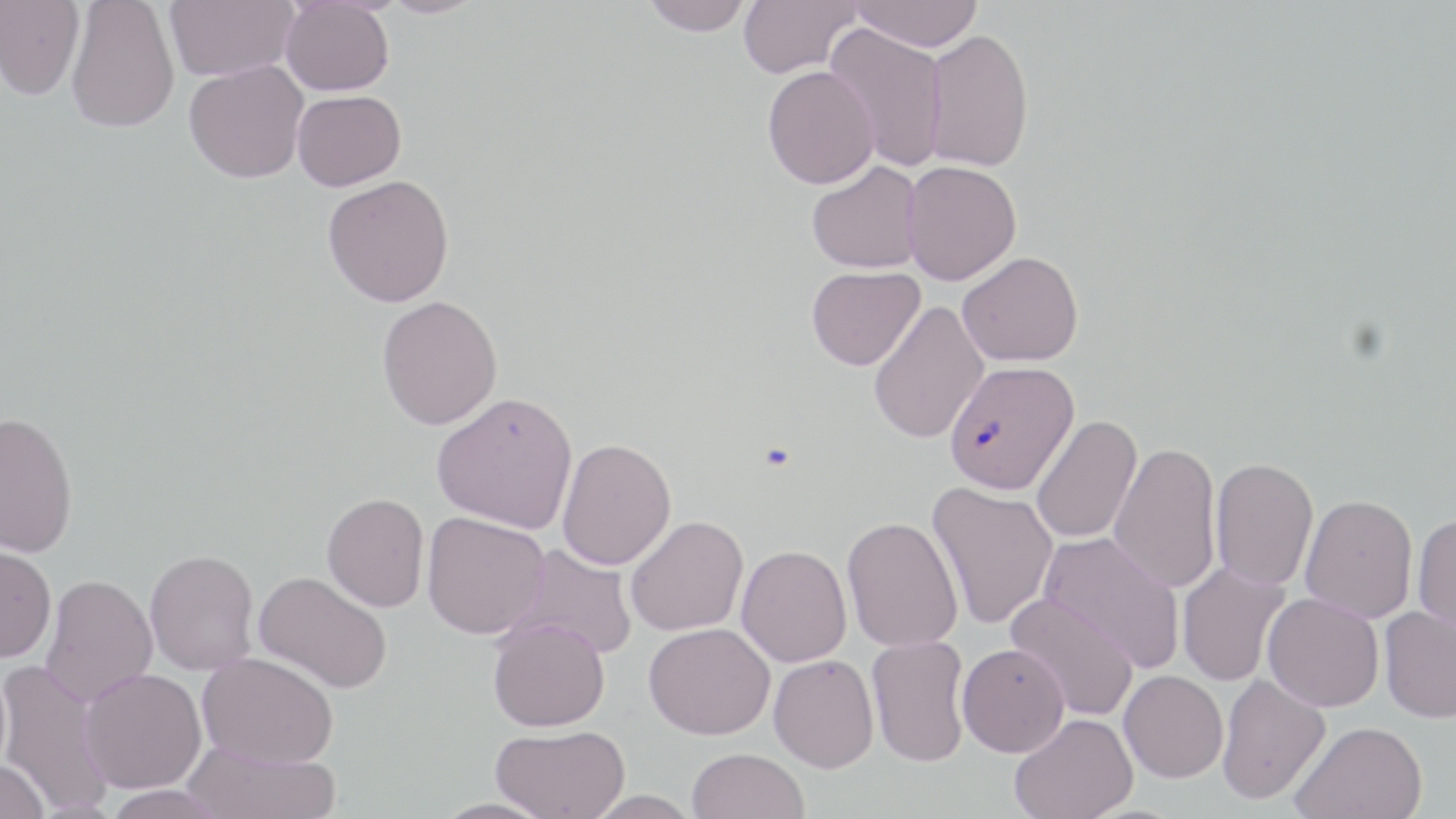

Approximate bounding boxes as named x1/y1/x2/y2 corners in pixels. Uninfected red blood cell locations: (x1=166, y1=0, x2=298, y2=81), (x1=377, y1=0, x2=486, y2=18), (x1=640, y1=0, x2=752, y2=36), (x1=738, y1=0, x2=861, y2=78), (x1=849, y1=0, x2=982, y2=52), (x1=0, y1=1, x2=85, y2=100), (x1=66, y1=1, x2=180, y2=133), (x1=281, y1=1, x2=394, y2=96), (x1=825, y1=22, x2=948, y2=173), (x1=923, y1=28, x2=1035, y2=172), (x1=184, y1=60, x2=309, y2=183), (x1=762, y1=65, x2=879, y2=189), (x1=292, y1=90, x2=406, y2=191), (x1=807, y1=161, x2=924, y2=274), (x1=902, y1=161, x2=1022, y2=285), (x1=322, y1=175, x2=455, y2=307), (x1=957, y1=251, x2=1083, y2=366), (x1=806, y1=266, x2=925, y2=370), (x1=377, y1=295, x2=503, y2=430), (x1=868, y1=300, x2=989, y2=444), (x1=432, y1=391, x2=578, y2=533), (x1=0, y1=412, x2=78, y2=558), (x1=1031, y1=415, x2=1142, y2=543), (x1=557, y1=437, x2=677, y2=570), (x1=1109, y1=441, x2=1221, y2=593), (x1=1210, y1=457, x2=1319, y2=591), (x1=927, y1=482, x2=1059, y2=630), (x1=322, y1=492, x2=429, y2=612), (x1=1300, y1=494, x2=1418, y2=623), (x1=421, y1=511, x2=549, y2=639), (x1=1412, y1=513, x2=1456, y2=637), (x1=624, y1=515, x2=748, y2=636), (x1=842, y1=517, x2=963, y2=652), (x1=1038, y1=531, x2=1185, y2=673), (x1=0, y1=544, x2=56, y2=662), (x1=506, y1=544, x2=638, y2=660), (x1=736, y1=545, x2=852, y2=667), (x1=144, y1=549, x2=260, y2=675), (x1=1177, y1=561, x2=1290, y2=687), (x1=253, y1=571, x2=392, y2=694), (x1=40, y1=573, x2=158, y2=707), (x1=1005, y1=592, x2=1140, y2=721), (x1=1262, y1=592, x2=1384, y2=712), (x1=1379, y1=605, x2=1456, y2=723), (x1=488, y1=617, x2=610, y2=731), (x1=643, y1=622, x2=775, y2=739), (x1=867, y1=634, x2=970, y2=767), (x1=956, y1=643, x2=1070, y2=757), (x1=197, y1=651, x2=338, y2=768), (x1=768, y1=654, x2=879, y2=773), (x1=0, y1=660, x2=114, y2=814), (x1=80, y1=668, x2=206, y2=793), (x1=1119, y1=670, x2=1227, y2=783), (x1=1216, y1=672, x2=1330, y2=805), (x1=1009, y1=713, x2=1138, y2=819), (x1=1290, y1=721, x2=1428, y2=818), (x1=490, y1=724, x2=630, y2=819), (x1=182, y1=740, x2=339, y2=819), (x1=687, y1=747, x2=808, y2=819), (x1=0, y1=760, x2=51, y2=819), (x1=101, y1=784, x2=229, y2=819), (x1=581, y1=790, x2=702, y2=817). Plasmodium falciparum-infected red blood cell locations: (x1=944, y1=360, x2=1080, y2=495). Slide-level diagnosis: Plasmodium falciparum. One field of a larger specimen. Light microscopy. Image is 1456×819 pixels. May-Grünwald-Giemsa stain. Thin blood film. 1000x magnification.